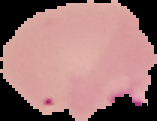
{
  "preparation": "thin blood film",
  "image_type": "segmented cell region on a black background",
  "image_size": "157×121 pixels",
  "malaria_status": "parasitized"
}